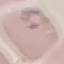

malaria_status: parasitized
image_type: cell patch, automatically extracted from a larger field of view and resized to 64 × 64 pixels
stain: Giemsa
preparation: thin smear
capture: smartphone through the microscope eyepiece